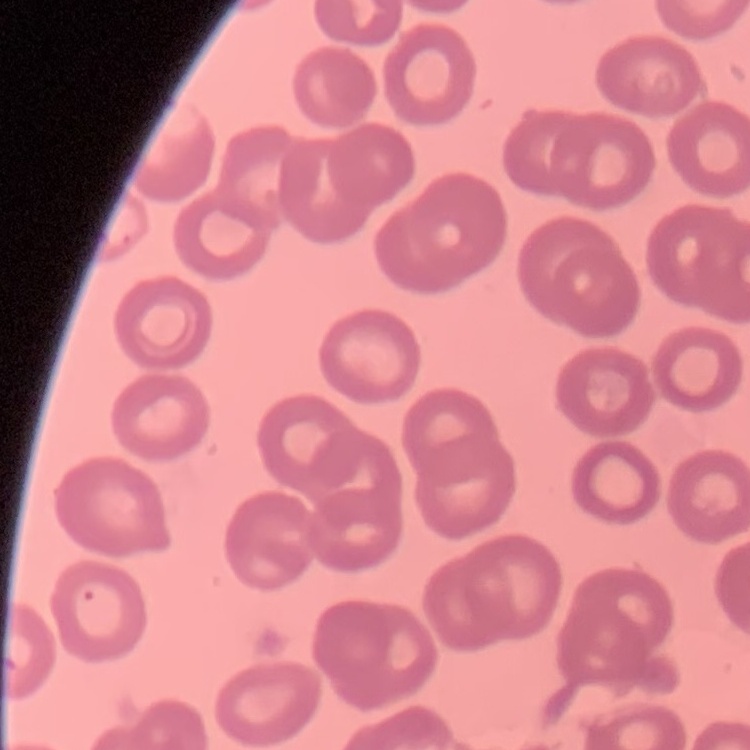

The red blood cells show no rouleaux formation. Thin blood smear. One tile cut from a larger photomicrograph. Field's or Giemsa stain.